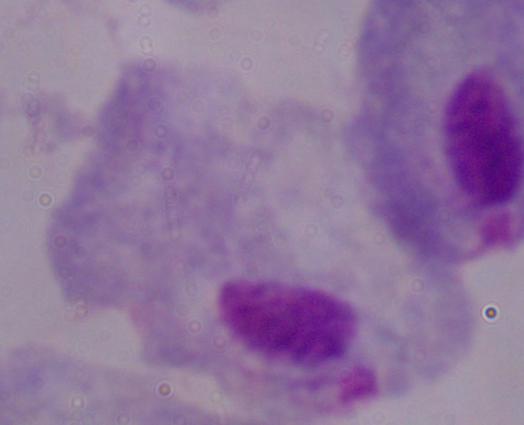

modality = photomicrograph
magnification = 1000x
identification = trichomonad